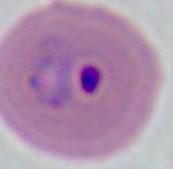
Summary:
  - Magnification: 400x or 1000x
  - Identification: Plasmodium
  - Modality: micrograph